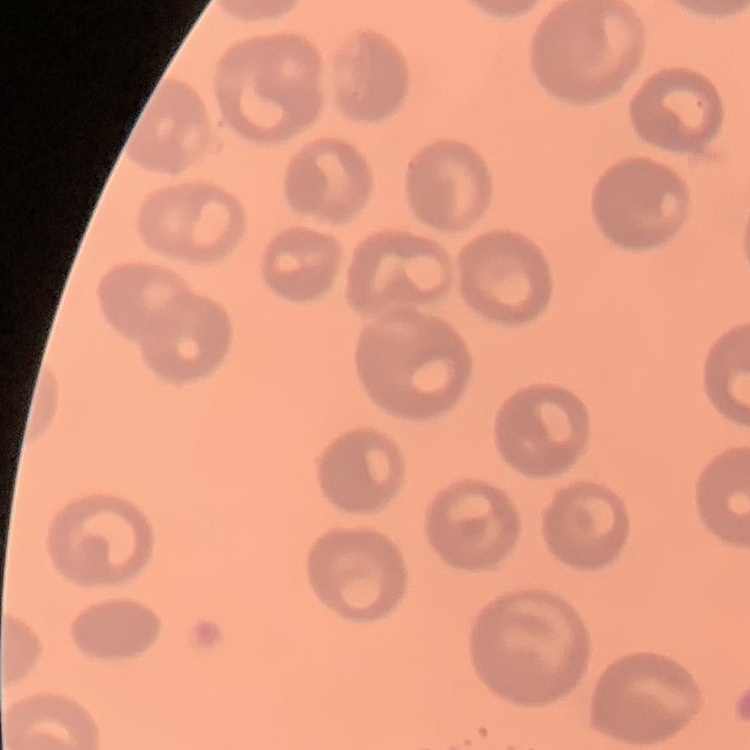

red blood cell morphology = no rouleaux formation
preparation = thin blood film
image type = square crop of a larger photomicrograph
stain = Field's or Giemsa